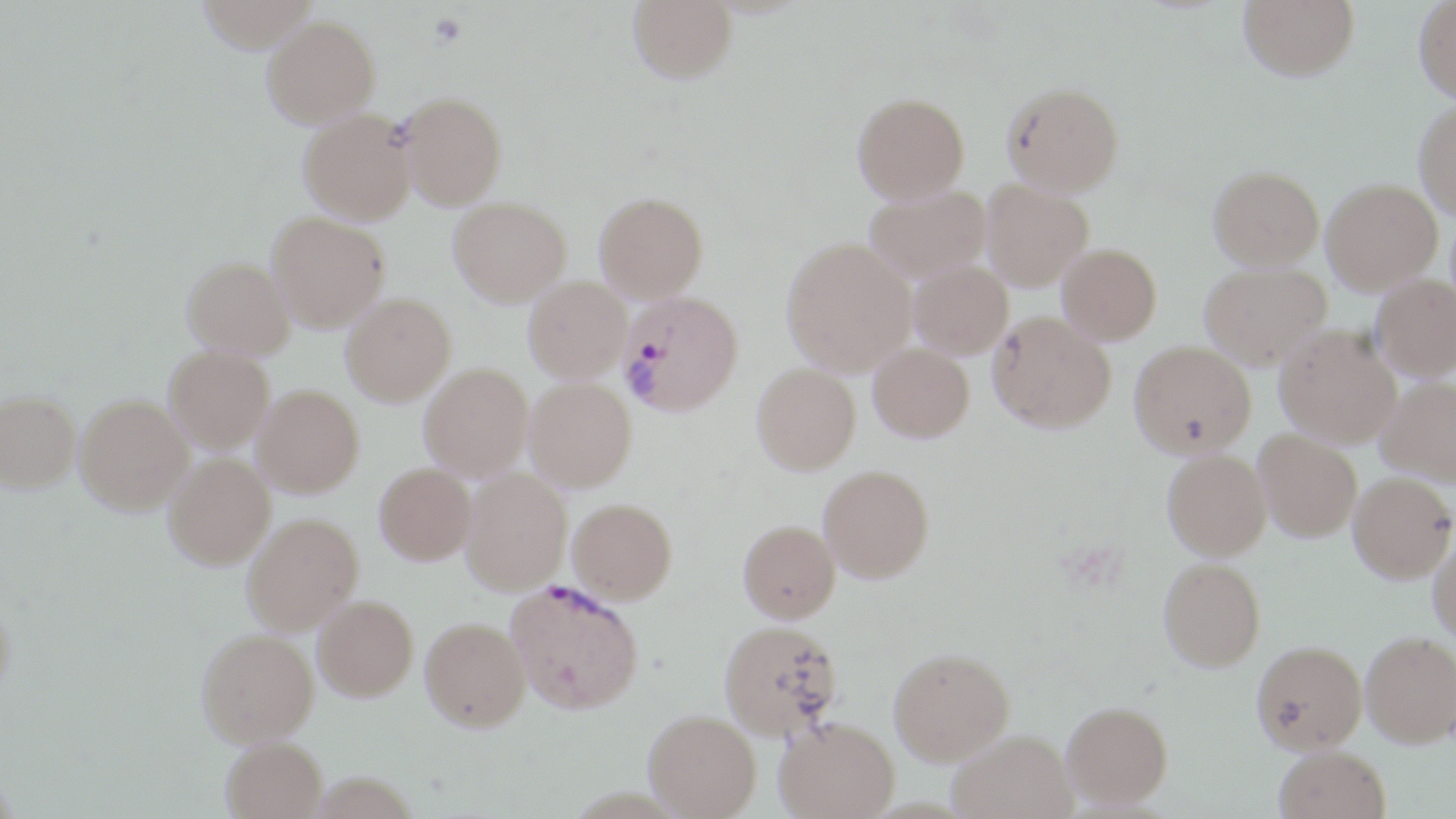
Approximate bounding boxes as (x1, y1, x2, y2) in pixels. Plasmodium vivax-infected red blood cell locations: (619, 290, 744, 416), (507, 580, 650, 720). Uninfected red blood cell locations: (195, 0, 318, 52), (628, 0, 736, 83), (1239, 0, 1358, 80), (1414, 1, 1456, 103), (263, 14, 380, 127), (1003, 83, 1123, 196), (398, 92, 507, 209), (853, 92, 969, 203), (1414, 100, 1456, 218), (299, 108, 416, 223), (1209, 165, 1324, 270), (1321, 179, 1441, 293), (982, 180, 1093, 290), (864, 184, 991, 282), (594, 192, 708, 302), (448, 197, 571, 306), (267, 212, 390, 331), (782, 238, 916, 375), (1058, 243, 1161, 344), (182, 257, 295, 359), (910, 260, 1012, 359), (1200, 262, 1332, 369), (1372, 275, 1456, 380), (524, 276, 632, 382), (341, 293, 456, 405), (988, 312, 1115, 432), (1275, 326, 1401, 446), (1129, 342, 1256, 456), (868, 343, 974, 442), (165, 345, 273, 452), (419, 363, 533, 479), (752, 363, 860, 474), (525, 377, 636, 491), (1377, 377, 1456, 485), (253, 386, 364, 497), (1, 392, 80, 492), (76, 394, 193, 513), (1254, 430, 1362, 542), (1163, 449, 1271, 559), (164, 453, 274, 569), (375, 463, 475, 564), (818, 465, 934, 582), (460, 469, 571, 594), (1349, 472, 1455, 583), (568, 497, 677, 603), (242, 513, 363, 634), (738, 519, 841, 622), (1429, 534, 1456, 647), (1158, 557, 1265, 670), (313, 595, 418, 701), (0, 600, 15, 702), (420, 617, 530, 731), (719, 620, 842, 738), (197, 629, 318, 746), (1361, 632, 1456, 747), (1252, 640, 1366, 753), (889, 648, 1014, 765), (1061, 701, 1173, 810), (644, 709, 760, 817), (775, 717, 899, 819), (948, 730, 1077, 819), (220, 737, 327, 819), (1273, 745, 1391, 819). Slide-level diagnosis: Plasmodium vivax. Image is 1456×819 pixels. Optical microscopy. May-Grünwald-Giemsa stain. 1000x magnification. One field of a larger specimen. Thin blood smear.